Assess this cell for malaria.
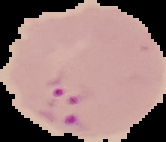
Parasitized.

image size = 166×142 pixels
image type = segmented cell region with the area outside set to black
preparation = thin blood film